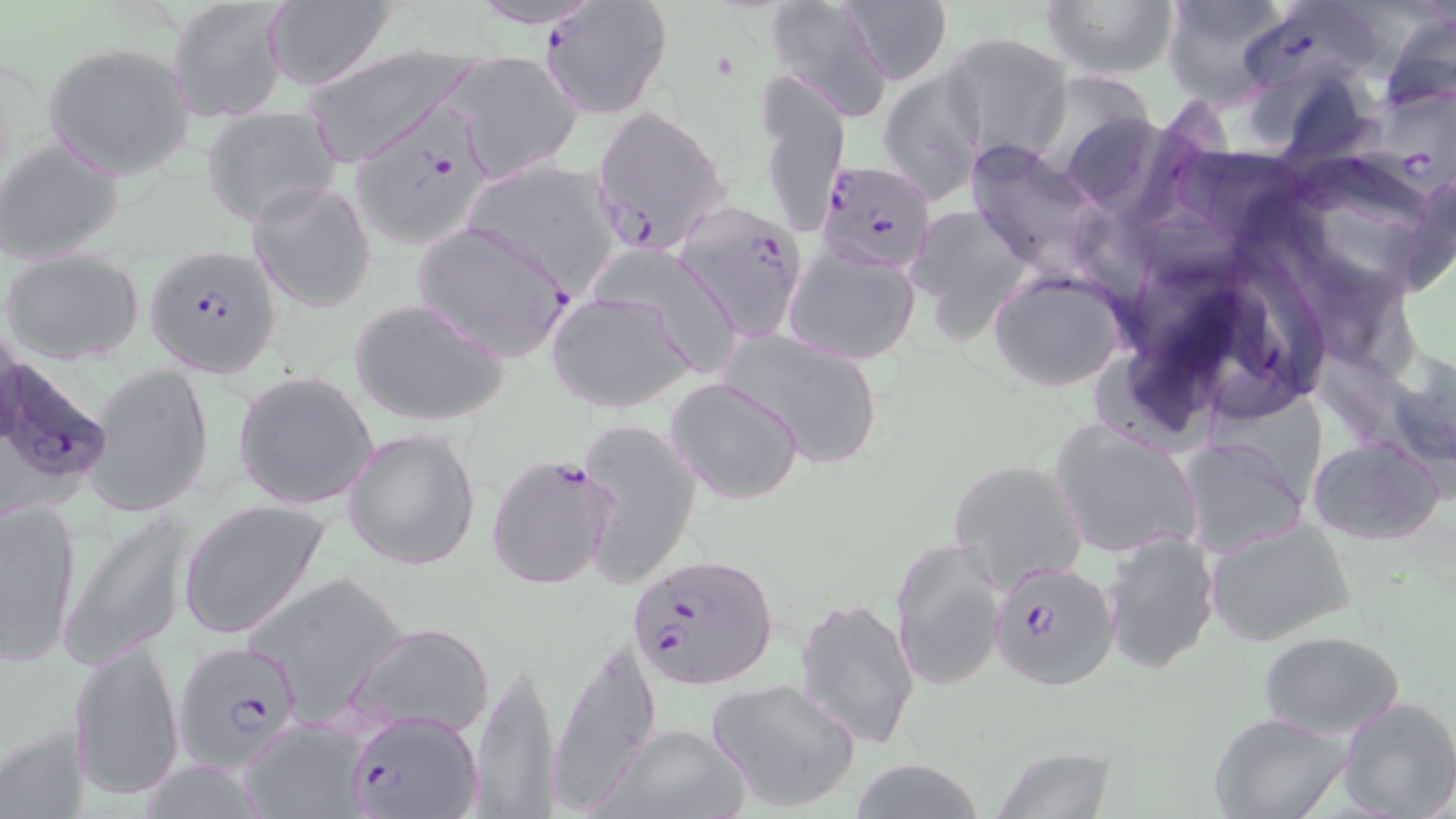

Summary:
  - Coordinate format: approximate bounding boxes as [x1, y1, x2, y2] in pixels
  - Uninfected red blood cell locations: [459, 0, 612, 30], [1040, 0, 1179, 81], [1158, 0, 1293, 107], [837, 1, 952, 84], [169, 2, 290, 124], [764, 2, 893, 119], [260, 4, 395, 90], [1375, 11, 1456, 113], [943, 32, 1073, 167], [42, 42, 195, 179], [302, 44, 483, 167], [447, 51, 582, 181], [880, 67, 989, 206], [751, 74, 847, 240], [201, 108, 343, 226], [0, 140, 123, 264], [961, 141, 1111, 279], [457, 158, 624, 293], [247, 180, 376, 313], [909, 207, 1029, 337], [783, 246, 921, 363], [3, 248, 146, 363], [991, 271, 1126, 391], [547, 291, 693, 414], [349, 297, 511, 427], [716, 326, 887, 469], [83, 363, 214, 517], [233, 370, 379, 510], [665, 377, 805, 504], [579, 418, 701, 585], [1050, 420, 1205, 558], [343, 427, 480, 568], [1179, 437, 1310, 557], [1306, 437, 1446, 545], [947, 457, 1088, 591], [0, 495, 83, 666], [177, 498, 333, 641], [59, 510, 193, 669], [1206, 517, 1357, 648], [1101, 530, 1221, 674], [889, 535, 1007, 692], [244, 568, 413, 718], [795, 596, 921, 748], [336, 621, 496, 741], [1259, 630, 1404, 739], [547, 637, 658, 806], [69, 639, 185, 801], [470, 655, 561, 813], [706, 677, 861, 811], [1337, 697, 1456, 819], [1209, 711, 1355, 819], [239, 721, 369, 818], [593, 722, 755, 819], [0, 723, 91, 818], [987, 746, 1118, 819], [847, 758, 988, 818]
  - Plasmodium falciparum-infected red blood cell locations: [539, 0, 672, 119], [1239, 4, 1393, 97], [1351, 93, 1456, 207], [589, 105, 731, 256], [352, 111, 493, 248], [816, 160, 936, 276], [675, 204, 808, 340], [411, 221, 573, 363], [144, 246, 281, 375], [5, 355, 113, 505], [486, 453, 614, 592], [626, 550, 779, 693], [988, 557, 1118, 689], [172, 641, 304, 774], [346, 708, 483, 819]
  - Slide-level diagnosis: Plasmodium falciparum
  - Stain: May-Grünwald-Giemsa
  - Field of view: one of a larger specimen
  - Preparation: thin blood film
  - Image size: 1456×819 pixels
  - Modality: optical microscopy
  - Magnification: 1000x